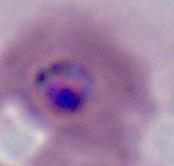

Summary:
  - Magnification: 400x or 1000x
  - Modality: micrograph
  - Identification: Plasmodium